Locate every Plasmodium parasite.
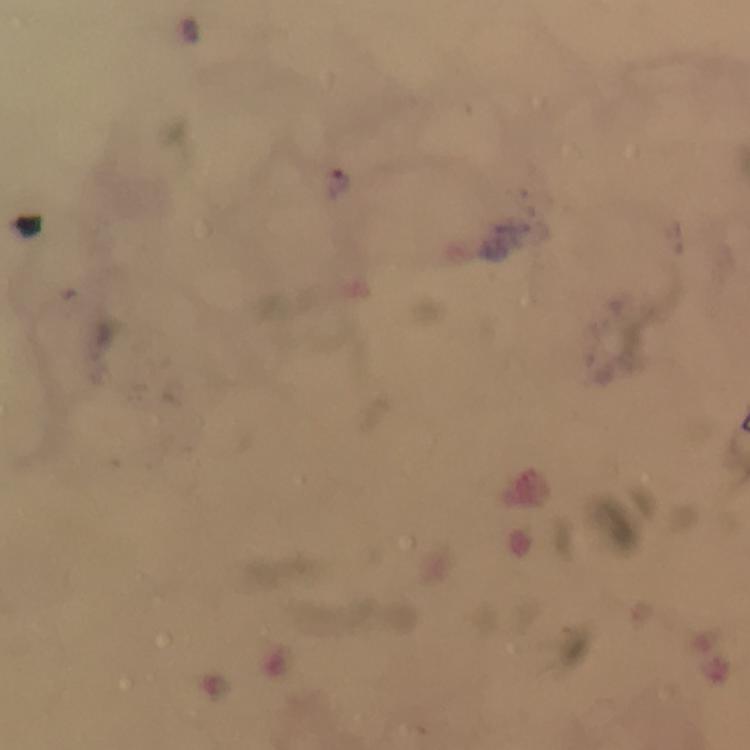

Approximate centers as [x, y] in pixels.
Plasmodium parasites: [337, 181].

Summary:
  - Magnification: 100x
  - Immersion oil: used
  - Capture: smartphone photograph through a microscope
  - Cropped from: one field of view
  - Image size: 750×750 pixels
  - Stain: Giemsa
  - Preparation: thick blood smear
  - Context: from a diagnostic examination for malaria